Comment on the morphology of the red blood cells.
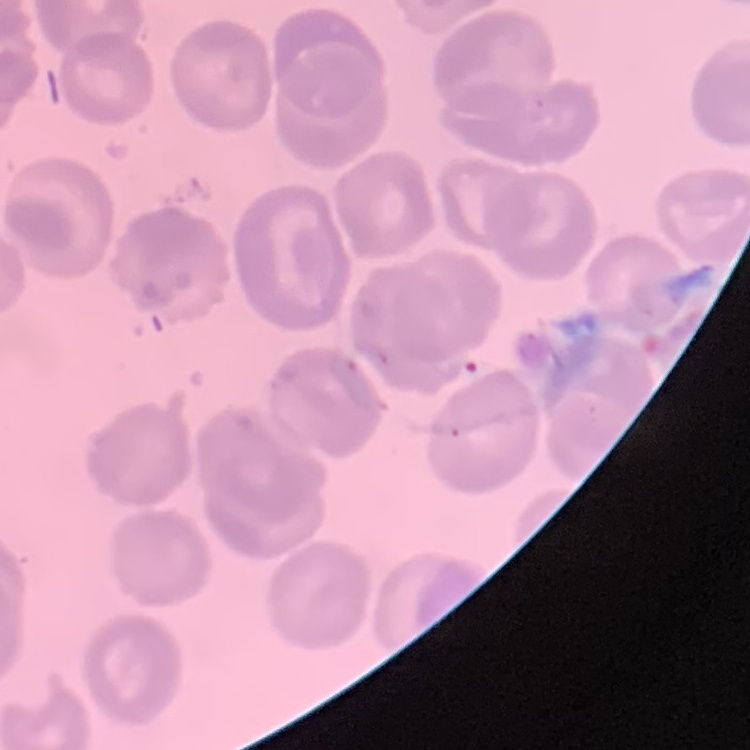

No rouleaux formation.

preparation = thin blood smear
stain = Field's or Giemsa
image type = one tile cut from a larger photomicrograph